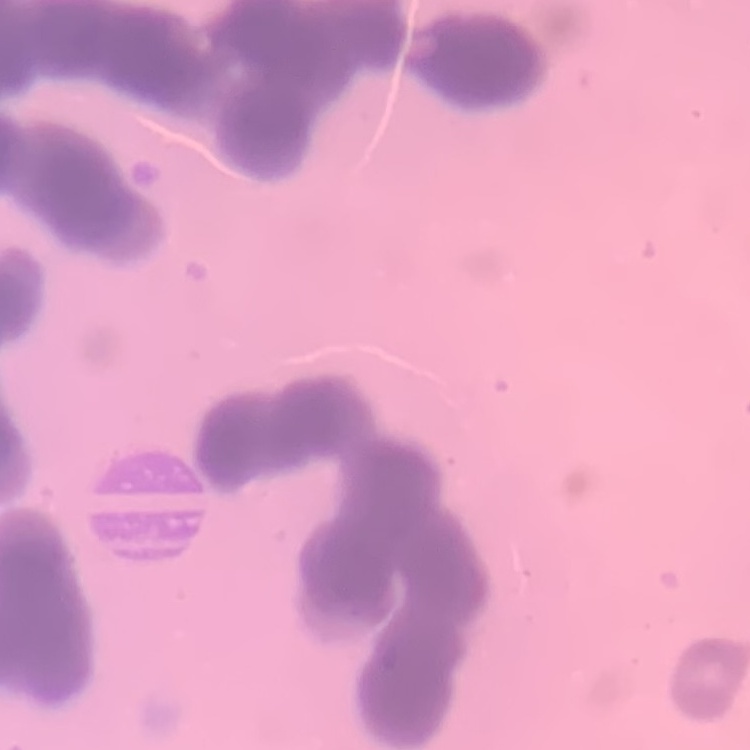
Summary:
  - Red blood cell morphology: rouleaux formation
  - Image type: square crop of a larger photomicrograph
  - Preparation: thin blood film
  - Stain: Field's or Giemsa